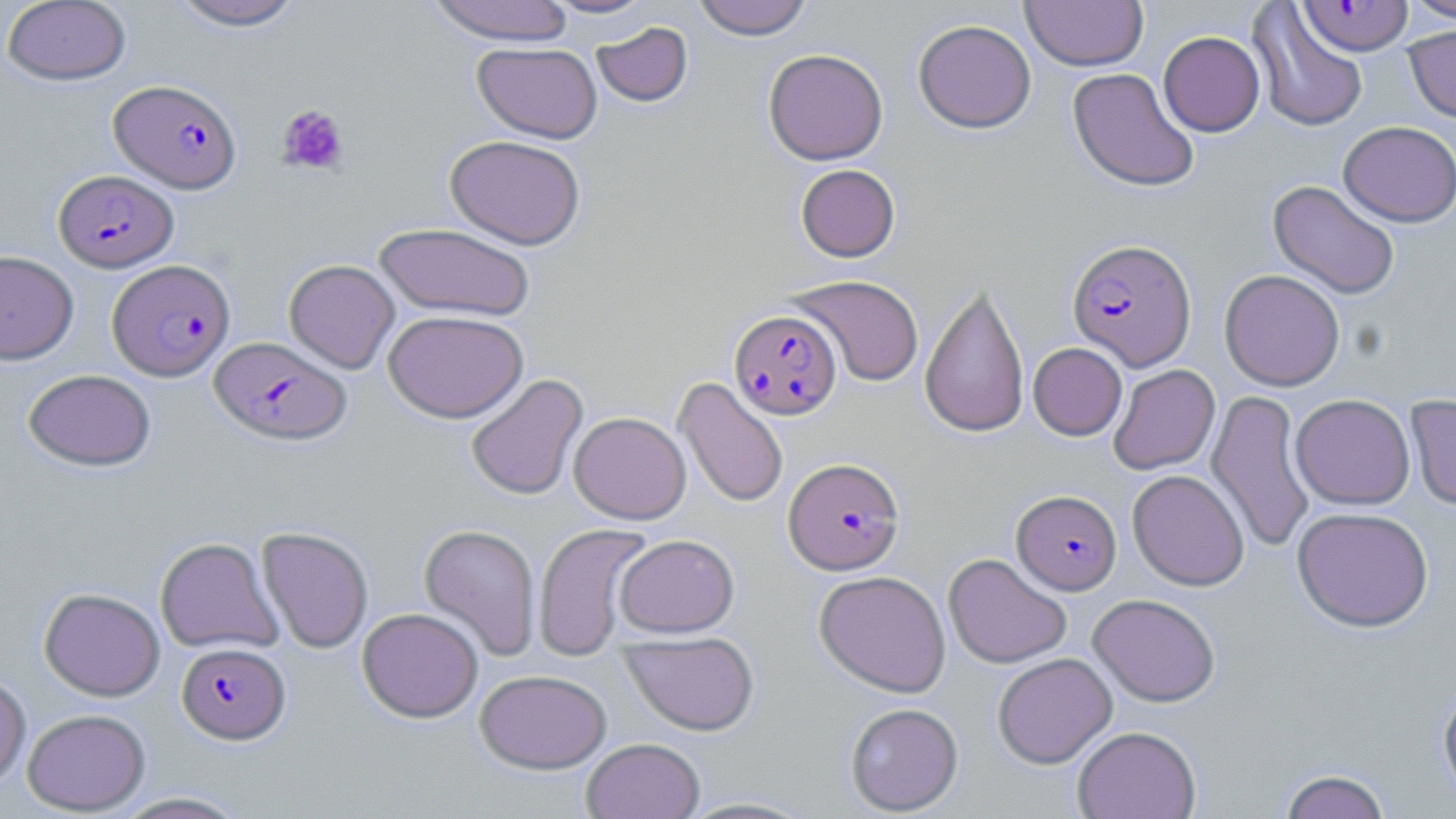
Summary:
  - Coordinate format: approximate bounding boxes as (x1,y1)-(x2,y2) corner pairs in pixels
  - Plasmodium falciparum-infected red blood cell locations: (1298,0)-(1413,56), (109,79)-(242,193), (53,170)-(178,272), (1067,239)-(1196,371), (108,259)-(235,381), (730,309)-(842,419), (209,336)-(351,445), (784,457)-(904,575), (1012,489)-(1122,594), (177,642)-(290,744)
  - Platelet locations: (276,104)-(350,176)
  - Uninfected red blood cell locations: (1,0)-(132,86), (166,0)-(306,30), (426,0)-(577,45), (543,0)-(657,18), (692,0)-(813,40), (1020,0)-(1149,71), (1402,0)-(1456,23), (1248,2)-(1369,133), (913,19)-(1036,133), (591,21)-(692,106), (1404,25)-(1456,122), (1158,31)-(1265,136), (472,42)-(602,143), (763,48)-(888,165), (1067,68)-(1200,192), (1339,120)-(1456,227), (445,134)-(586,250), (796,164)-(900,262), (1268,180)-(1401,300), (374,223)-(536,321), (0,250)-(79,363), (283,259)-(400,373), (1219,269)-(1345,391), (788,275)-(924,387), (920,280)-(1030,439), (383,309)-(528,423), (1028,342)-(1127,440), (1108,364)-(1220,475), (23,369)-(155,471), (465,373)-(588,501), (674,377)-(789,509), (1206,389)-(1317,554), (1290,393)-(1415,509), (1405,393)-(1456,510), (569,411)-(691,524), (1127,469)-(1250,591), (1291,506)-(1434,632), (532,522)-(654,661), (419,523)-(542,661), (257,526)-(374,654), (615,534)-(739,637), (155,537)-(283,654), (943,553)-(1072,669), (814,570)-(951,698), (39,587)-(165,701), (1088,593)-(1221,706), (357,607)-(484,723), (620,631)-(759,735), (992,652)-(1117,768), (474,669)-(612,774), (0,673)-(31,790), (1438,682)-(1456,803), (845,702)-(963,815), (22,709)-(151,815), (1072,726)-(1201,818), (581,737)-(705,819), (1277,768)-(1393,818), (109,791)-(254,818), (675,796)-(822,818)
  - Slide-level diagnosis: Plasmodium falciparum
  - Image size: 1456×819 pixels
  - Field of view: one of a larger specimen
  - Preparation: thin blood smear
  - Magnification: 1000x
  - Stain: May-Grünwald-Giemsa
  - Modality: light microscopy